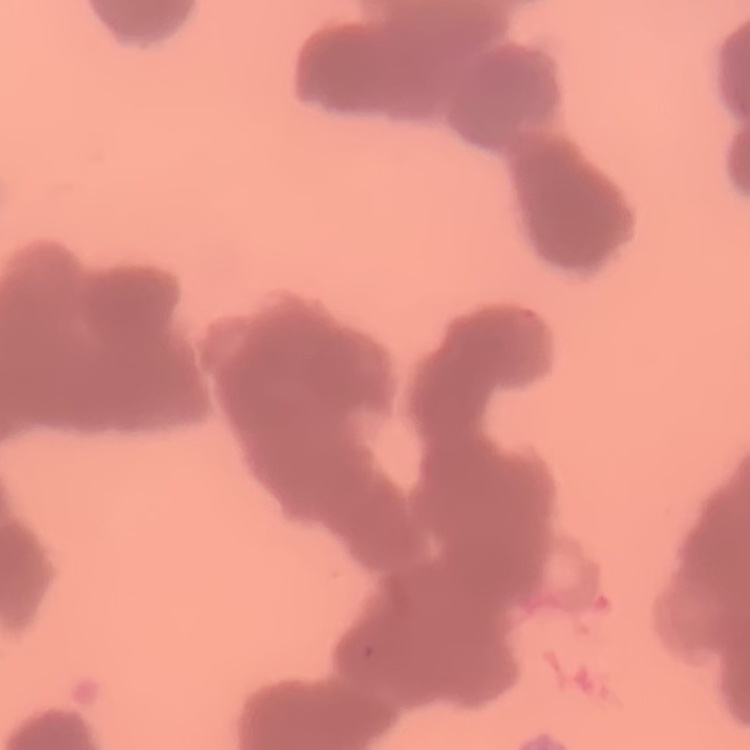
erythrocyte_morphology: rouleaux formation
stain: Field's or Giemsa
image_type: square crop of a larger photomicrograph
preparation: thin blood film